Locate and identify every blood parasite.
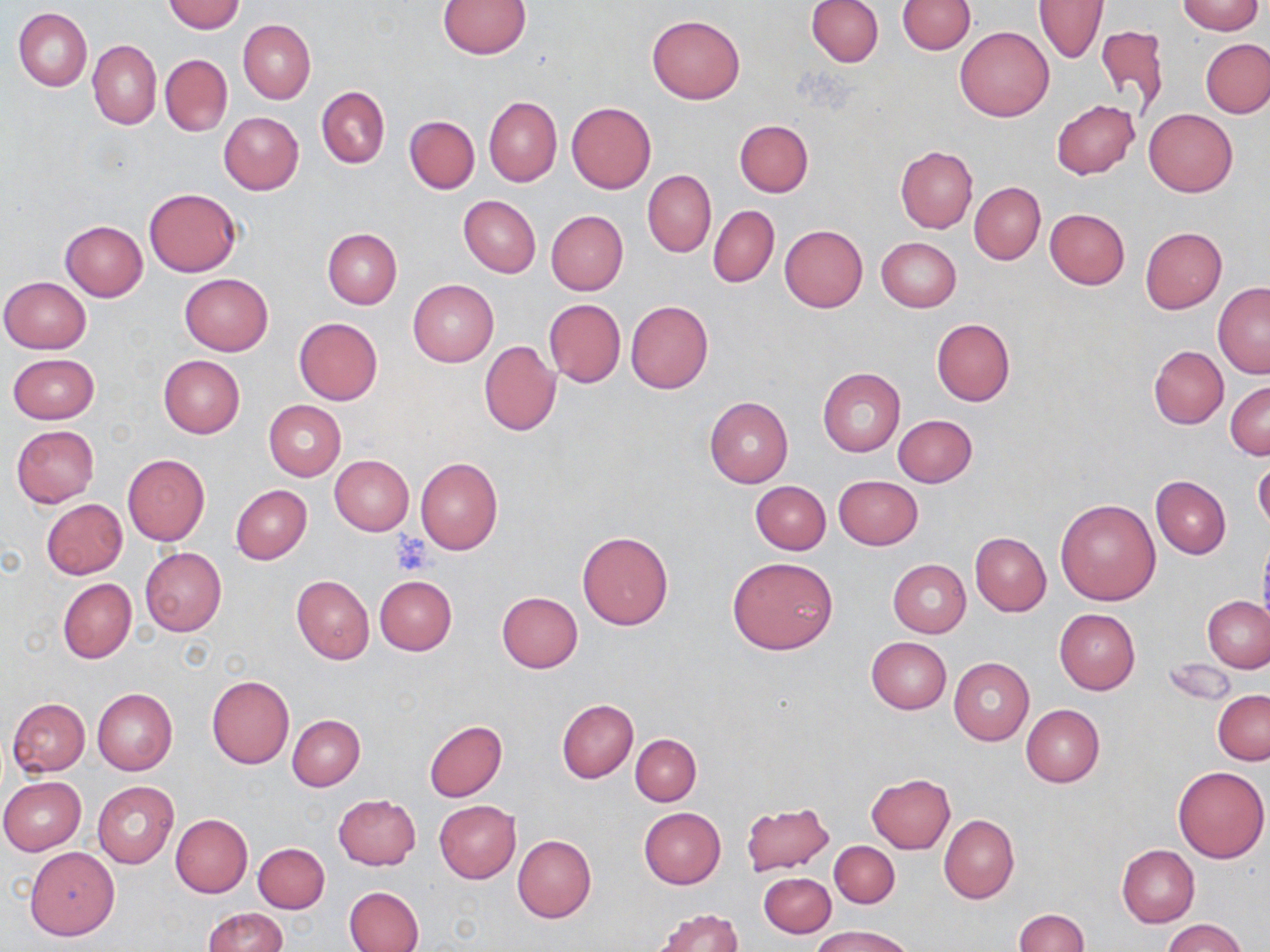
No blood parasites seen.

Summary:
  - Coordinate format: approximate bounding boxes as (x1, y1, x2, y2) in pixels
  - Uninfected red blood cell locations: (806, 0, 883, 67), (897, 0, 975, 55), (164, 1, 245, 33), (439, 1, 531, 58), (1034, 1, 1108, 63), (1178, 1, 1263, 35), (14, 8, 91, 92), (646, 15, 745, 103), (238, 19, 315, 102), (1094, 24, 1169, 115), (955, 26, 1054, 121), (1202, 38, 1270, 117), (88, 40, 161, 129), (160, 54, 232, 137), (317, 86, 389, 168), (484, 96, 562, 186), (1051, 99, 1140, 179), (566, 102, 656, 193), (1143, 109, 1239, 197), (219, 112, 303, 195), (404, 116, 479, 193), (735, 120, 813, 197), (896, 146, 977, 232), (643, 170, 715, 257), (970, 182, 1046, 264), (144, 188, 241, 278), (458, 195, 541, 277), (708, 206, 779, 288), (1044, 208, 1130, 289), (546, 211, 628, 295), (60, 220, 148, 300), (779, 224, 868, 312), (322, 227, 402, 309), (1140, 227, 1227, 314), (876, 237, 961, 312), (180, 273, 273, 355), (1, 276, 90, 353), (408, 279, 498, 366), (1213, 281, 1270, 379), (544, 298, 626, 387), (626, 301, 713, 393), (294, 317, 382, 405), (931, 318, 1015, 406), (478, 340, 561, 436), (1149, 346, 1228, 428), (7, 353, 99, 424), (159, 355, 244, 438), (818, 368, 905, 456), (1226, 380, 1270, 460), (705, 397, 794, 488), (264, 400, 345, 480), (893, 415, 977, 487), (10, 424, 99, 506), (123, 454, 209, 545), (330, 455, 413, 535), (1254, 456, 1270, 533), (415, 458, 503, 554), (834, 475, 922, 549), (1151, 476, 1231, 559), (751, 481, 831, 555), (231, 484, 312, 564), (1054, 498, 1159, 605), (41, 499, 128, 579), (577, 530, 673, 631), (970, 533, 1051, 615), (1257, 536, 1270, 634), (140, 547, 226, 636), (728, 557, 838, 655), (888, 559, 971, 637), (291, 575, 374, 663), (375, 575, 457, 655), (58, 579, 136, 663), (497, 592, 583, 673), (1203, 596, 1269, 672), (1054, 608, 1140, 694), (865, 636, 952, 713), (949, 657, 1034, 747), (1162, 657, 1237, 706), (206, 676, 294, 769), (92, 688, 177, 775), (1213, 690, 1270, 764), (7, 698, 90, 776), (557, 699, 638, 782), (1021, 703, 1105, 787), (288, 714, 365, 790), (424, 720, 506, 802), (631, 734, 700, 806), (1172, 765, 1269, 862), (865, 773, 954, 853), (0, 777, 86, 855), (93, 782, 177, 869), (333, 794, 421, 870), (434, 800, 521, 883), (741, 801, 834, 875), (638, 808, 726, 889), (171, 814, 252, 897), (939, 815, 1019, 903), (513, 835, 596, 923), (830, 841, 899, 908), (253, 842, 329, 913), (1117, 844, 1199, 928), (25, 847, 119, 939), (760, 873, 835, 937), (344, 886, 423, 952), (202, 906, 288, 951), (654, 907, 743, 952), (1013, 909, 1087, 952), (1161, 917, 1246, 952), (815, 925, 911, 952)
  - Platelet locations: (388, 533, 434, 573)
  - Slide-level diagnosis: negative for blood parasites
  - Preparation: thin blood smear
  - Magnification: 1000x
  - Modality: light microscopy
  - Image size: 1270×952 pixels
  - Stain: May-Grünwald-Giemsa
  - Field of view: single